Locate and identify every blood parasite.
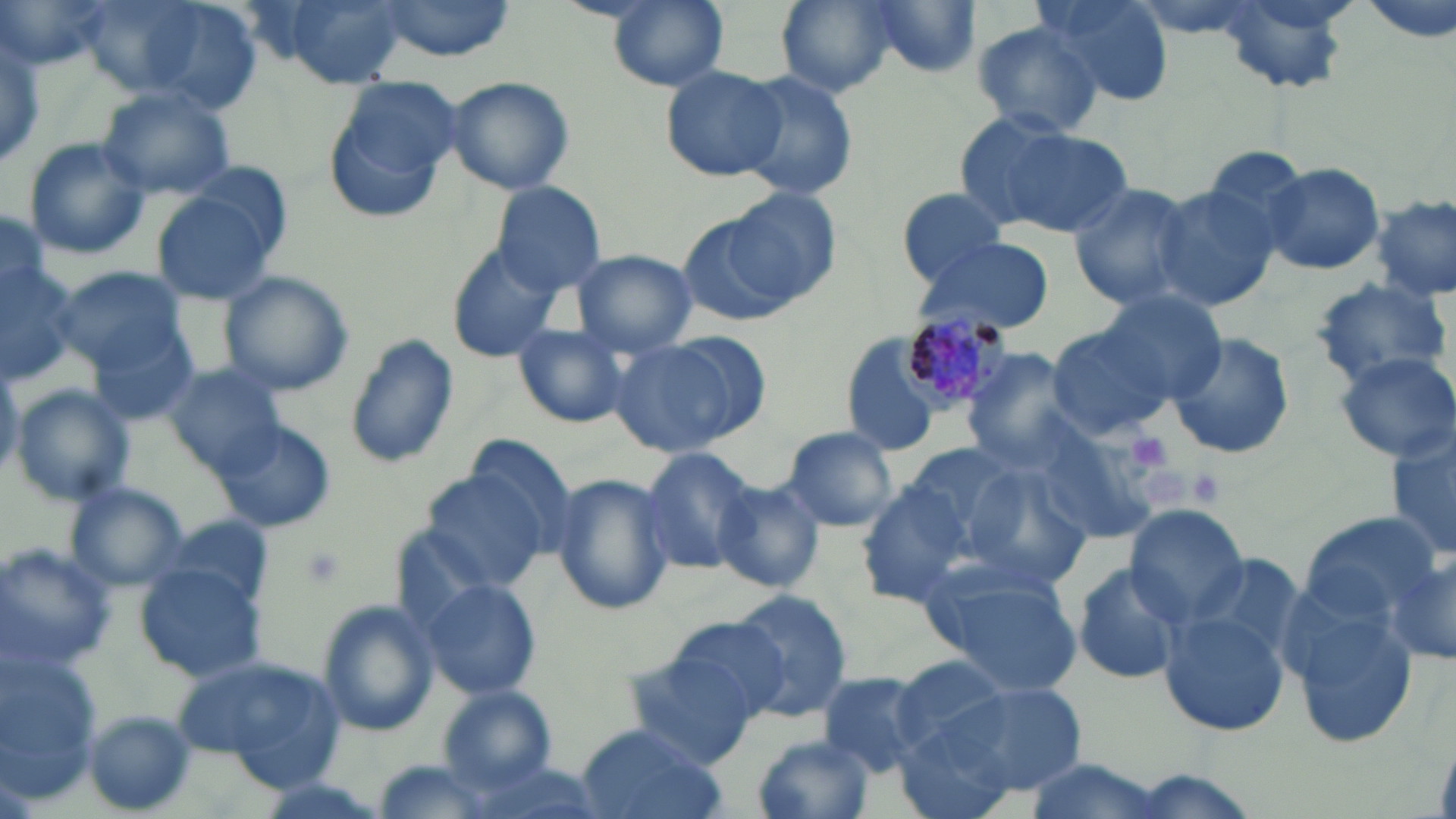
Approximate bounding boxes as (x1, y1, x2, y2) in pixels.
Plasmodium malariae-infected red blood cells: (894, 300, 1014, 418).
No Plasmodium falciparum, Plasmodium ovale, Plasmodium vivax, Babesia divergens, or Trypanosoma brucei observed.

slide-level diagnosis = Plasmodium malariae
modality = optical microscopy
platelet locations = approximate bounding boxes as (x1, y1, x2, y2) in pixels: (1124, 431, 1175, 476), (1176, 466, 1229, 509)
uninfected red blood cell locations = approximate bounding boxes as (x1, y1, x2, y2) in pixels: (1, 0, 112, 70), (69, 0, 262, 110), (274, 0, 411, 87), (375, 0, 517, 58), (607, 0, 729, 91), (775, 0, 897, 97), (1032, 0, 1174, 108), (859, 1, 985, 79), (970, 21, 1104, 138), (0, 22, 46, 172), (659, 65, 787, 181), (730, 68, 859, 204), (444, 75, 577, 196), (323, 79, 459, 224), (97, 87, 235, 201), (957, 114, 1132, 240), (20, 136, 152, 261), (1260, 161, 1385, 277), (490, 180, 608, 294), (1067, 182, 1202, 312), (1151, 182, 1283, 313), (147, 184, 285, 307), (896, 186, 1015, 288), (730, 187, 843, 301), (1371, 193, 1455, 303), (0, 203, 52, 305), (674, 209, 799, 328), (915, 236, 1054, 335), (442, 245, 558, 363), (571, 251, 699, 357), (0, 254, 82, 386), (55, 265, 188, 373), (218, 270, 354, 396), (1311, 276, 1452, 386), (1090, 289, 1230, 404), (512, 323, 632, 429), (1043, 324, 1173, 442), (90, 329, 200, 427), (1165, 331, 1297, 462), (343, 333, 460, 472), (606, 334, 763, 461), (837, 334, 948, 458), (960, 348, 1081, 468), (1332, 353, 1455, 462), (165, 363, 286, 476), (9, 384, 136, 506), (216, 420, 335, 532), (1387, 423, 1456, 567), (1033, 424, 1164, 539), (778, 425, 899, 532), (467, 435, 572, 546), (894, 439, 1033, 561), (639, 448, 760, 575), (962, 465, 1093, 590), (422, 470, 552, 591), (550, 472, 673, 617), (713, 478, 824, 594), (856, 480, 993, 611), (64, 482, 189, 592), (1124, 505, 1249, 625), (1296, 512, 1441, 634), (155, 517, 276, 609), (0, 542, 116, 674), (1380, 542, 1456, 670), (1180, 547, 1307, 674), (917, 557, 1084, 693), (1071, 561, 1188, 688), (134, 564, 266, 681), (418, 577, 541, 699), (726, 589, 851, 718), (317, 602, 440, 740), (1288, 603, 1419, 749), (1162, 610, 1292, 734), (665, 614, 797, 728), (0, 650, 104, 793), (620, 650, 761, 768), (174, 653, 344, 787), (885, 654, 1018, 757), (816, 668, 932, 774), (942, 681, 1088, 796), (442, 688, 556, 787), (80, 710, 201, 817), (573, 723, 721, 819), (895, 726, 1019, 819), (750, 733, 876, 819), (1016, 757, 1171, 819)
image size = 1456×819 pixels
magnification = 1000x
field of view = one of a larger specimen
preparation = thin blood smear
stain = May-Grünwald-Giemsa